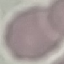
Malaria status: uninfected. Acquired by smartphone through the microscope eyepiece. Giemsa stain. Cell patch, automatically extracted from a larger field of view and resized to 64 × 64 pixels. Thin blood film.